Report the malaria status of this cell.
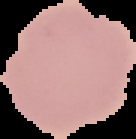

It is uninfected.

{
  "preparation": "thin blood film",
  "image_type": "segmented cell region with the area outside set to black",
  "image_size": "136×139 pixels"
}